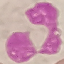

malaria status = uninfected
preparation = thin smear
stain = Giemsa
image type = automatically extracted cell patch, resized to 64 × 64 pixels
capture = smartphone camera at the microscope eyepiece